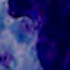
A white blood cell is shown. Photomicrograph. Captured at 1000x magnification.